Identify the blood parasite species.
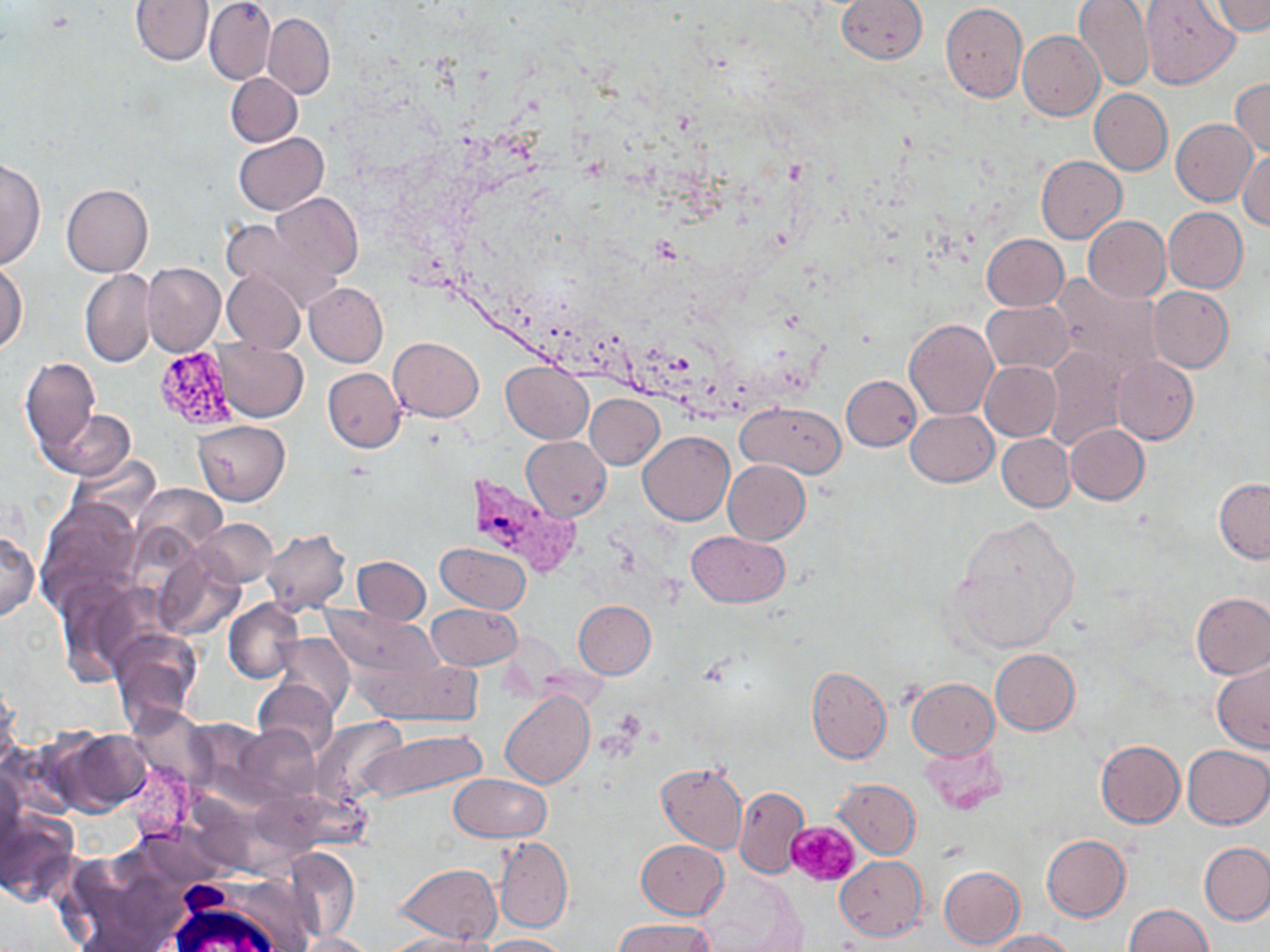
Plasmodium vivax.

platelet_locations: 'approximate bounding boxes as [x1, y1, x2, y2] in pixels: [788, 820, 859, 886]'
plasmodium_vivax_infected_red_blood_cell_locations: 'approximate bounding boxes as [x1, y1, x2, y2] in pixels: [467, 473, 580, 579]'
stain: May-Grünwald-Giemsa
field_of_view: single
modality: optical microscopy
image_size: 1270×952 pixels
uninfected_red_blood_cell_locations: 'approximate bounding boxes as [x1, y1, x2, y2] in pixels: [130, 0, 214, 65], [204, 0, 276, 85], [837, 0, 927, 64], [1074, 0, 1156, 93], [1141, 1, 1240, 89], [1208, 1, 1268, 35], [940, 2, 1027, 101], [263, 13, 335, 99], [1018, 30, 1104, 120], [225, 72, 302, 147], [1230, 78, 1270, 157], [1089, 88, 1172, 175], [1171, 119, 1257, 207], [234, 132, 328, 215], [1238, 149, 1269, 229], [1036, 155, 1127, 245], [0, 159, 45, 271], [61, 184, 152, 277], [268, 193, 363, 281], [1163, 207, 1248, 293], [1083, 215, 1171, 302], [222, 217, 339, 313], [981, 234, 1068, 311], [0, 262, 28, 353], [142, 262, 224, 355], [80, 269, 157, 368], [223, 271, 305, 352], [1051, 275, 1164, 376], [304, 282, 388, 367], [1147, 286, 1234, 373], [981, 301, 1074, 375], [903, 318, 997, 419], [389, 337, 483, 421], [214, 339, 308, 422], [1043, 346, 1128, 452], [1112, 355, 1198, 445], [20, 358, 100, 453], [980, 361, 1061, 441], [501, 362, 593, 443], [322, 368, 406, 451], [841, 375, 921, 450], [585, 394, 664, 469], [737, 402, 846, 477], [43, 409, 134, 481], [905, 410, 997, 486], [1065, 424, 1149, 504], [638, 431, 734, 527], [997, 434, 1075, 511], [522, 436, 611, 521], [67, 454, 161, 530], [723, 459, 810, 544], [1214, 478, 1270, 562], [133, 483, 225, 557], [35, 497, 145, 611], [947, 515, 1082, 655], [197, 518, 276, 587], [260, 528, 352, 615], [687, 530, 789, 605], [0, 532, 39, 621], [435, 541, 532, 614], [154, 550, 246, 639], [352, 556, 431, 625], [56, 577, 158, 685], [1191, 592, 1270, 678], [223, 598, 304, 683], [573, 600, 656, 679], [426, 603, 523, 671], [322, 605, 443, 682], [108, 630, 202, 730], [269, 632, 355, 717], [990, 649, 1080, 735], [358, 653, 484, 726], [1211, 658, 1270, 753], [806, 665, 891, 764], [907, 677, 999, 759], [253, 678, 338, 758], [0, 682, 20, 766], [500, 690, 593, 789], [128, 707, 215, 791], [186, 718, 270, 793], [312, 718, 406, 804], [236, 724, 322, 804], [359, 727, 487, 803], [52, 728, 151, 815], [1095, 741, 1184, 827], [1182, 744, 1270, 830], [125, 761, 198, 840], [656, 761, 747, 852], [0, 770, 25, 858], [449, 773, 549, 841], [832, 778, 921, 859], [734, 786, 809, 877], [0, 808, 80, 906], [137, 823, 226, 890], [1042, 834, 1130, 922], [493, 836, 572, 933], [635, 839, 729, 918], [1198, 842, 1270, 926], [286, 847, 360, 940], [835, 856, 926, 940], [397, 863, 502, 945], [940, 865, 1024, 951], [695, 869, 804, 950], [1123, 904, 1213, 952], [610, 919, 715, 952], [983, 929, 1075, 951], [296, 931, 376, 951], [384, 934, 492, 952], [479, 934, 569, 951]'
preparation: thin blood film
magnification: 1000x